Identify the parasite.
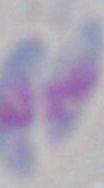
This is Toxoplasma gondii.

Summary:
  - Magnification: 1000x
  - Modality: micrograph